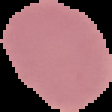
Segmented cell region on a black background. Result: negative for malaria parasites. Image is 112×112 pixels. From a thin blood smear.